Identify the parasite.
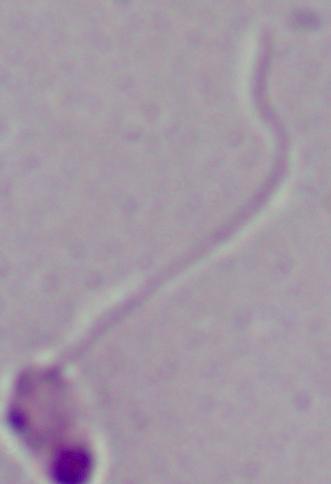
This is Leishmania.

Summary:
  - Modality: micrograph
  - Magnification: 1000x